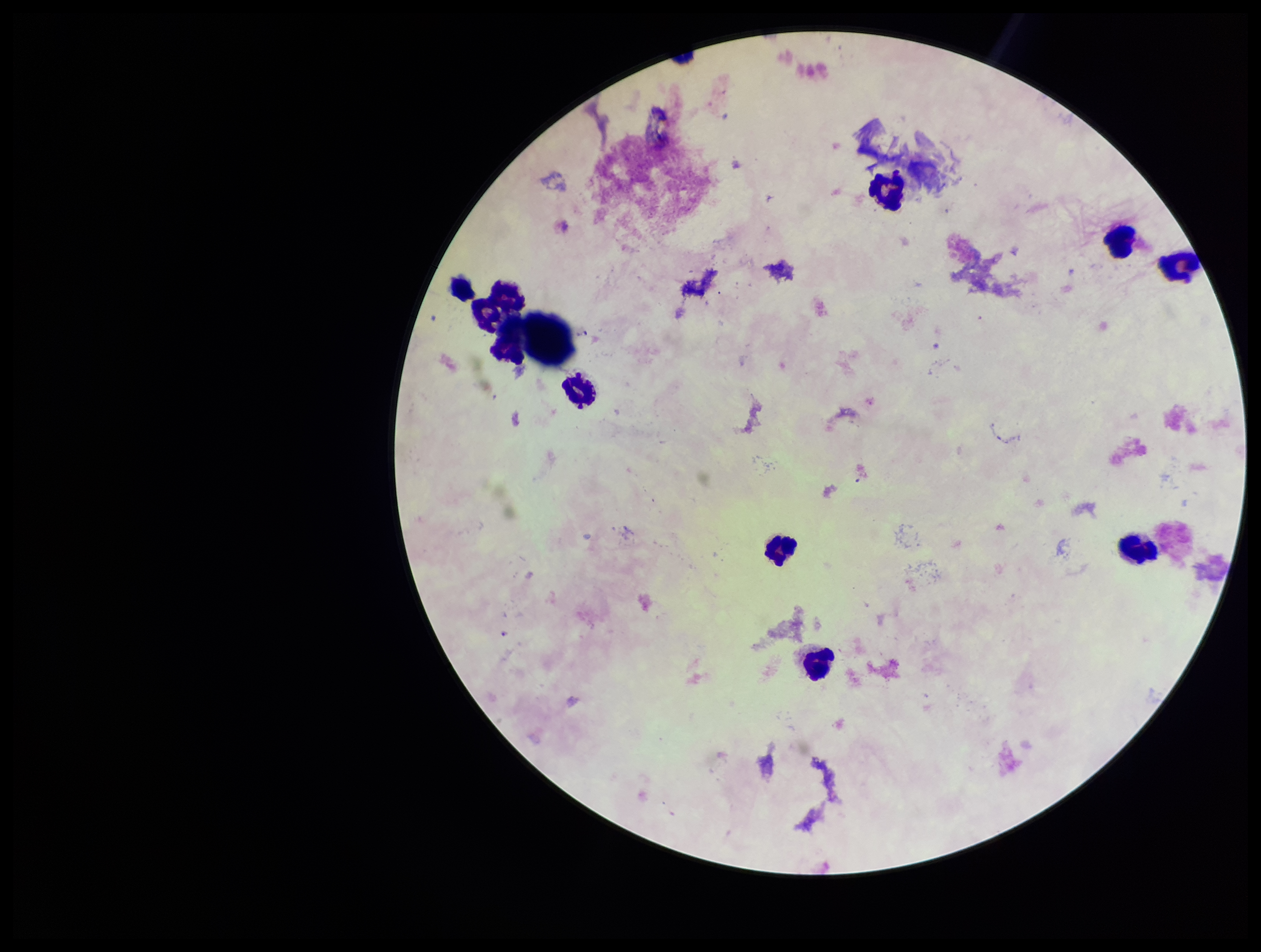

Summary:
  - Capture: smartphone photograph through the microscope eyepiece
  - Image size: 1261×952 pixels
  - Parasite count: 0
  - Plasmodium parasites: none detected
  - Preparation: thick
  - Patient malaria status: infected
  - Species reported for this patient: Plasmodium falciparum
  - Leukocyte count: 10
  - Stain: Giemsa
  - Field of view: single